Describe the morphology of the red blood cells.
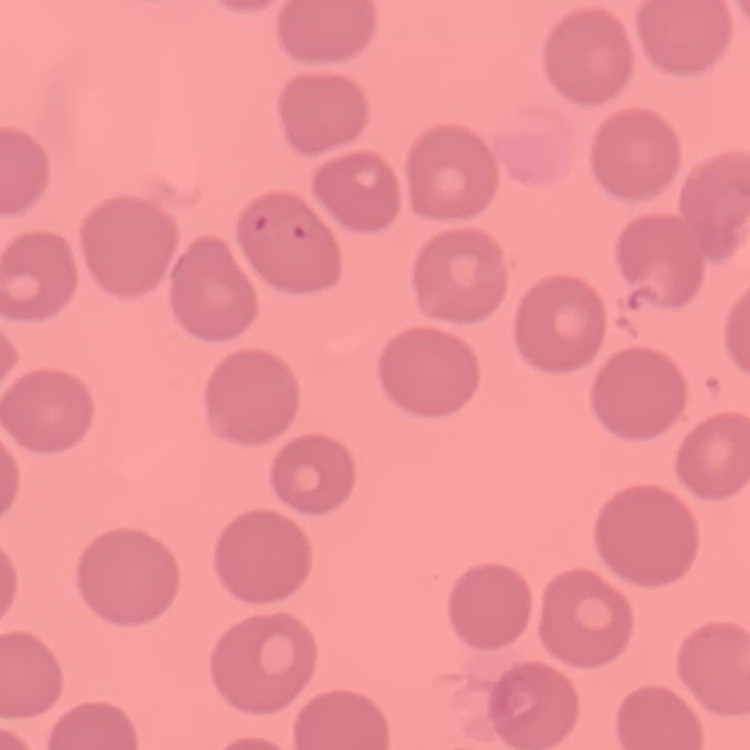
No rouleaux formation.

Summary:
  - Image type: one tile cut from a larger photomicrograph
  - Preparation: thin blood smear
  - Stain: Field's or Giemsa